Assess the morphology of the erythrocytes.
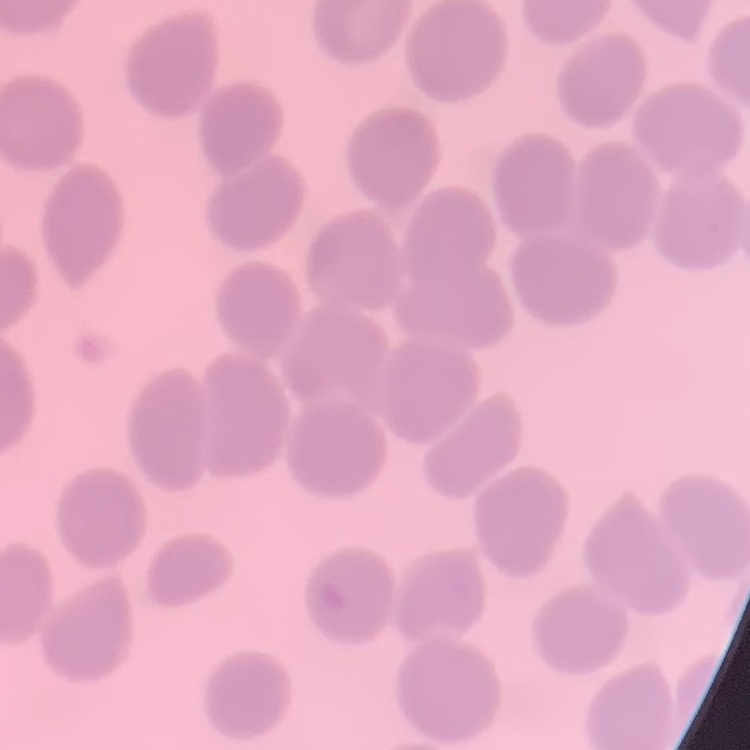

No rouleaux formation.

stain = Field's or Giemsa
image type = square crop of a larger photomicrograph
preparation = thin peripheral smear